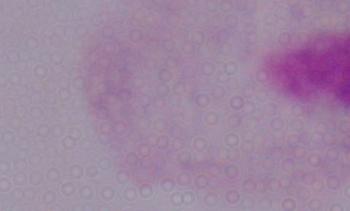

Summary:
  - Magnification: 1000x
  - Modality: micrograph
  - Identification: trichomonad